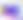 Toxoplasma gondii is shown. Micrograph. Captured at 400x magnification.